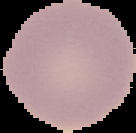

Summary:
  - Image type: segmented cell region with the area outside set to black
  - Preparation: thin blood smear
  - Malaria status: uninfected
  - Image size: 136×133 pixels